Locate every blood parasite and identify its species.
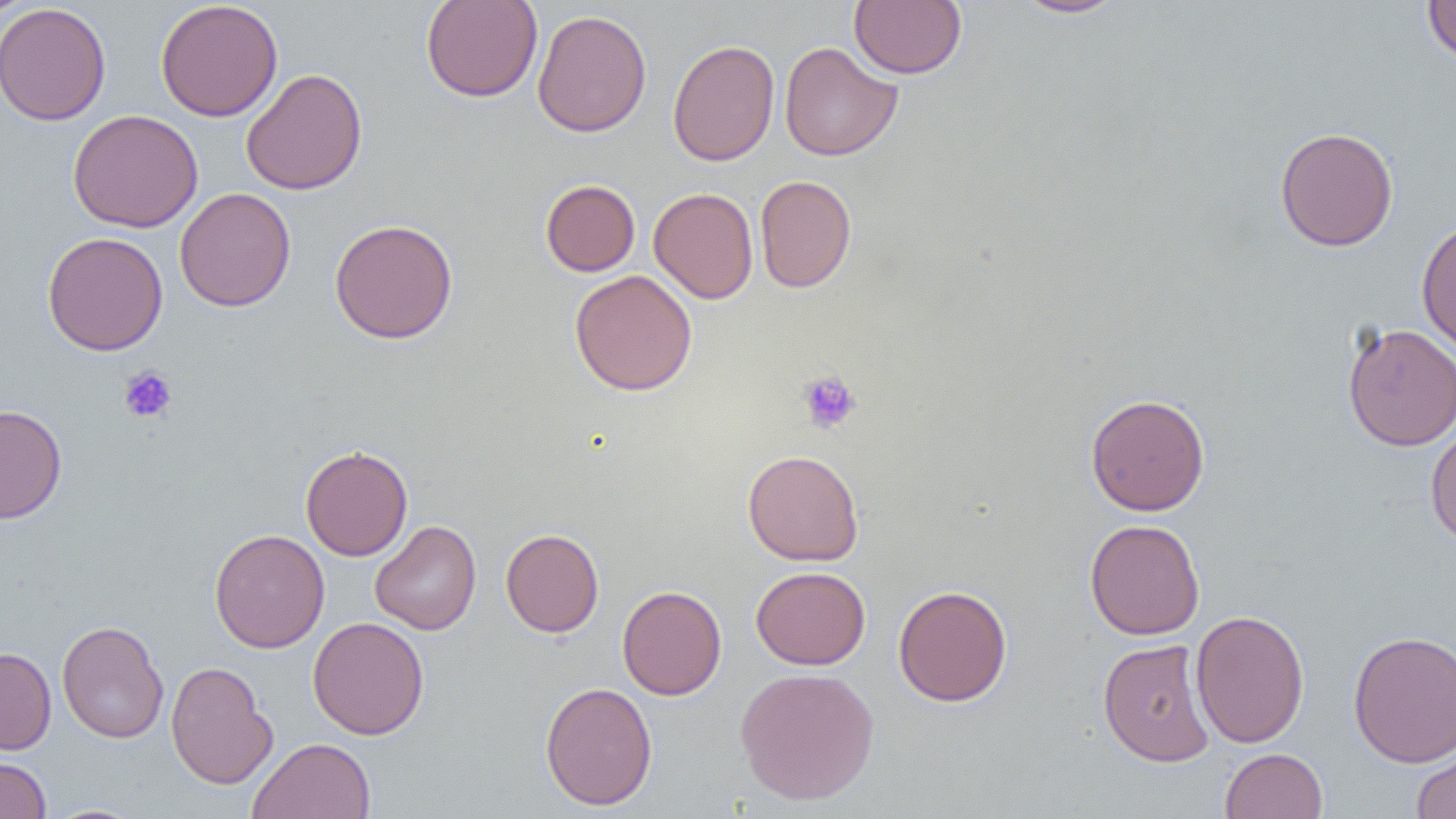

No blood parasites observed.

Summary:
  - Coordinate format: approximate bounding boxes as (x1, y1, x2, y2) in pixels
  - Platelet locations: (119, 366, 178, 423), (797, 370, 862, 434)
  - Uninfected red blood cell locations: (1, 0, 35, 19), (420, 0, 543, 102), (849, 0, 967, 79), (1010, 0, 1127, 19), (1422, 0, 1456, 64), (155, 1, 283, 122), (0, 3, 111, 126), (532, 9, 652, 137), (667, 39, 780, 167), (779, 42, 902, 161), (241, 68, 367, 195), (67, 109, 203, 232), (1274, 126, 1399, 252), (754, 175, 856, 292), (540, 179, 640, 276), (175, 187, 296, 312), (648, 187, 758, 304), (1416, 216, 1456, 357), (329, 218, 458, 344), (42, 232, 168, 355), (569, 270, 698, 396), (1341, 322, 1456, 452), (1085, 393, 1210, 516), (0, 404, 67, 524), (1425, 421, 1456, 546), (300, 444, 413, 561), (742, 449, 864, 566), (1084, 518, 1204, 640), (370, 520, 482, 635), (209, 528, 330, 653), (500, 528, 604, 637), (750, 566, 870, 670), (617, 585, 727, 700), (892, 585, 1013, 707), (1191, 608, 1310, 749), (308, 616, 429, 740), (57, 620, 169, 743), (1347, 630, 1456, 767), (1097, 638, 1215, 766), (0, 647, 56, 755), (165, 661, 276, 789), (734, 666, 879, 806), (540, 680, 657, 810), (248, 737, 376, 819), (1410, 746, 1456, 818), (1219, 748, 1328, 818), (0, 757, 51, 819)
  - Slide-level diagnosis: no evidence of blood parasites
  - Field of view: single
  - Image size: 1456×819 pixels
  - Magnification: 1000x
  - Preparation: thin blood film
  - Modality: light microscopy